Name the parasite shown.
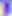

Toxoplasma gondii.

400x magnification. Micrograph.